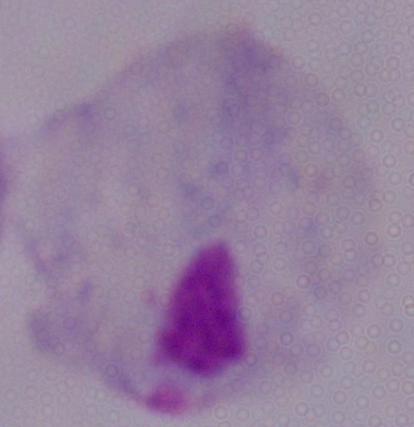

Summary:
  - Magnification: 1000x
  - Identification: trichomonad
  - Modality: micrograph